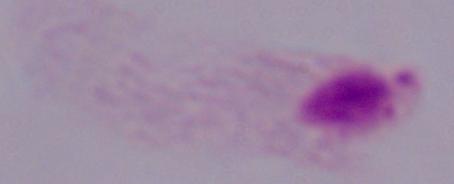

Photomicrograph. Captured at 1000x magnification. A trichomonad is shown.